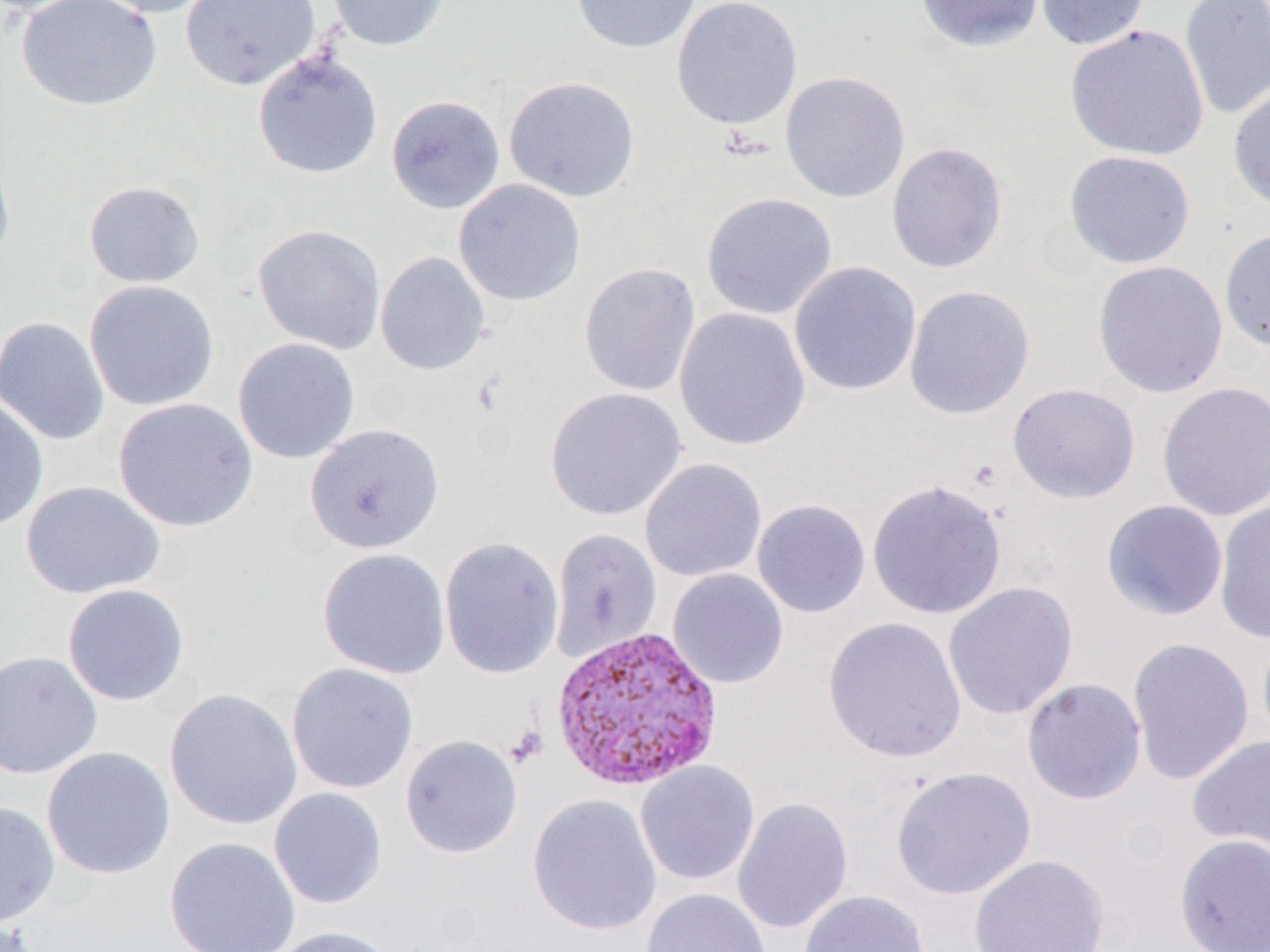
Summary:
  - Coordinate format: approximate bounding boxes as [x1, y1, x2, y2] in pixels
  - Uninfected red blood cell locations: [15, 0, 162, 112], [85, 0, 220, 18], [180, 0, 322, 91], [326, 0, 452, 52], [570, 0, 703, 54], [671, 0, 803, 131], [915, 0, 1045, 53], [1034, 0, 1150, 51], [1179, 0, 1270, 120], [1064, 24, 1209, 162], [253, 50, 383, 179], [779, 70, 911, 204], [503, 75, 640, 203], [1228, 81, 1270, 214], [385, 94, 506, 214], [885, 142, 1008, 274], [0, 144, 17, 274], [1063, 150, 1195, 269], [453, 179, 586, 306], [83, 180, 205, 289], [700, 192, 838, 319], [252, 223, 386, 355], [1219, 229, 1270, 352], [374, 251, 490, 376], [1093, 260, 1228, 398], [579, 261, 701, 397], [789, 261, 922, 396], [84, 279, 220, 412], [904, 285, 1035, 420], [674, 307, 811, 452], [0, 317, 111, 445], [232, 338, 361, 464], [1157, 382, 1270, 521], [1007, 383, 1140, 504], [544, 387, 687, 522], [0, 395, 49, 533], [112, 397, 259, 533], [304, 423, 445, 554], [639, 458, 767, 584], [867, 479, 1008, 620], [20, 481, 165, 600], [752, 499, 871, 618], [1101, 499, 1229, 621], [1213, 500, 1270, 644], [549, 528, 662, 662], [439, 536, 564, 679], [316, 548, 451, 680], [667, 568, 789, 689], [942, 581, 1079, 721], [61, 583, 191, 707], [823, 616, 967, 763], [1256, 628, 1270, 755], [1126, 637, 1255, 786], [0, 650, 103, 779], [286, 662, 419, 794], [1021, 677, 1147, 805], [164, 688, 302, 830], [399, 734, 523, 858], [1187, 735, 1270, 861], [40, 746, 175, 879], [635, 760, 761, 885], [890, 766, 1037, 900], [268, 787, 388, 909], [527, 794, 663, 937], [732, 797, 853, 934], [0, 801, 61, 928], [1173, 833, 1270, 952], [163, 836, 301, 952], [969, 853, 1110, 951], [641, 888, 773, 952], [799, 890, 930, 952], [0, 919, 49, 952], [266, 926, 398, 952]
  - Platelet locations: [506, 724, 548, 768]
  - Plasmodium vivax-infected red blood cell locations: [550, 624, 723, 792]
  - Slide-level diagnosis: Plasmodium vivax
  - Image size: 1270×952 pixels
  - Magnification: 1000x
  - Modality: light microscopy
  - Preparation: thin blood film
  - Field of view: single